Locate every blood parasite and identify its species.
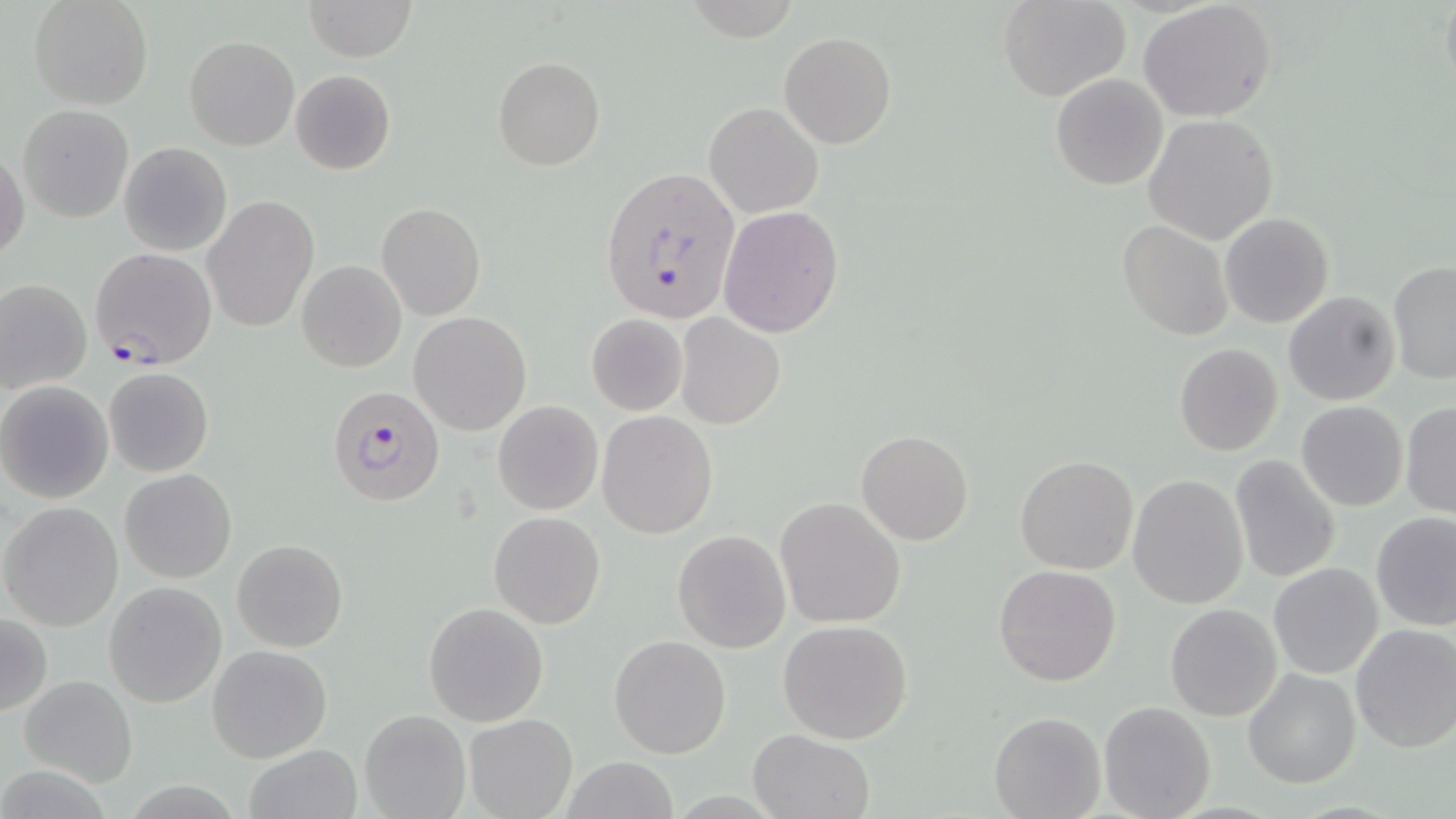
Approximate bounding boxes as [x1, y1, x2, y2] in pixels.
Plasmodium falciparum-infected red blood cells: [600, 166, 740, 327], [89, 247, 217, 369], [327, 384, 447, 507].
No Plasmodium ovale, Plasmodium malariae, Plasmodium vivax, Babesia divergens, or Trypanosoma brucei observed.

Summary:
  - Uninfected red blood cell locations: [29, 0, 153, 110], [301, 0, 417, 61], [1000, 0, 1130, 102], [1138, 0, 1279, 121], [779, 31, 896, 149], [184, 36, 300, 152], [493, 57, 605, 171], [290, 69, 396, 175], [1049, 73, 1169, 191], [705, 102, 823, 218], [17, 105, 134, 223], [1142, 114, 1279, 243], [119, 142, 232, 256], [1, 147, 28, 262], [204, 196, 319, 331], [377, 201, 486, 320], [719, 205, 843, 337], [1220, 212, 1334, 329], [1116, 219, 1233, 340], [297, 260, 406, 373], [1387, 262, 1456, 384], [0, 279, 92, 393], [1283, 291, 1400, 405], [408, 311, 532, 435], [585, 313, 690, 416], [675, 313, 785, 429], [1173, 343, 1283, 457], [104, 367, 214, 477], [0, 382, 114, 504], [1296, 401, 1407, 512], [1400, 401, 1456, 520], [494, 402, 604, 515], [597, 410, 719, 539], [856, 430, 973, 546], [1228, 454, 1342, 586], [1014, 455, 1139, 575], [120, 468, 237, 583], [1128, 475, 1249, 610], [776, 497, 907, 628], [1, 502, 124, 631], [1370, 510, 1456, 631], [488, 511, 606, 628], [672, 529, 792, 653], [231, 538, 348, 653], [1268, 563, 1383, 679], [993, 565, 1122, 686], [104, 582, 226, 708], [422, 602, 549, 727], [1164, 603, 1283, 721], [0, 615, 51, 717], [776, 619, 914, 744], [1350, 623, 1456, 753], [608, 635, 732, 758], [208, 645, 332, 762], [1242, 668, 1360, 788], [19, 674, 138, 788], [1099, 701, 1217, 819], [359, 709, 471, 819], [988, 711, 1105, 818], [463, 712, 577, 818], [746, 729, 875, 819], [244, 743, 362, 819], [561, 756, 678, 819]
  - Slide-level diagnosis: Plasmodium falciparum
  - Magnification: 1000x
  - Modality: light microscopy
  - Field of view: single
  - Preparation: thin blood smear
  - Stain: May-Grünwald-Giemsa
  - Image size: 1456×819 pixels